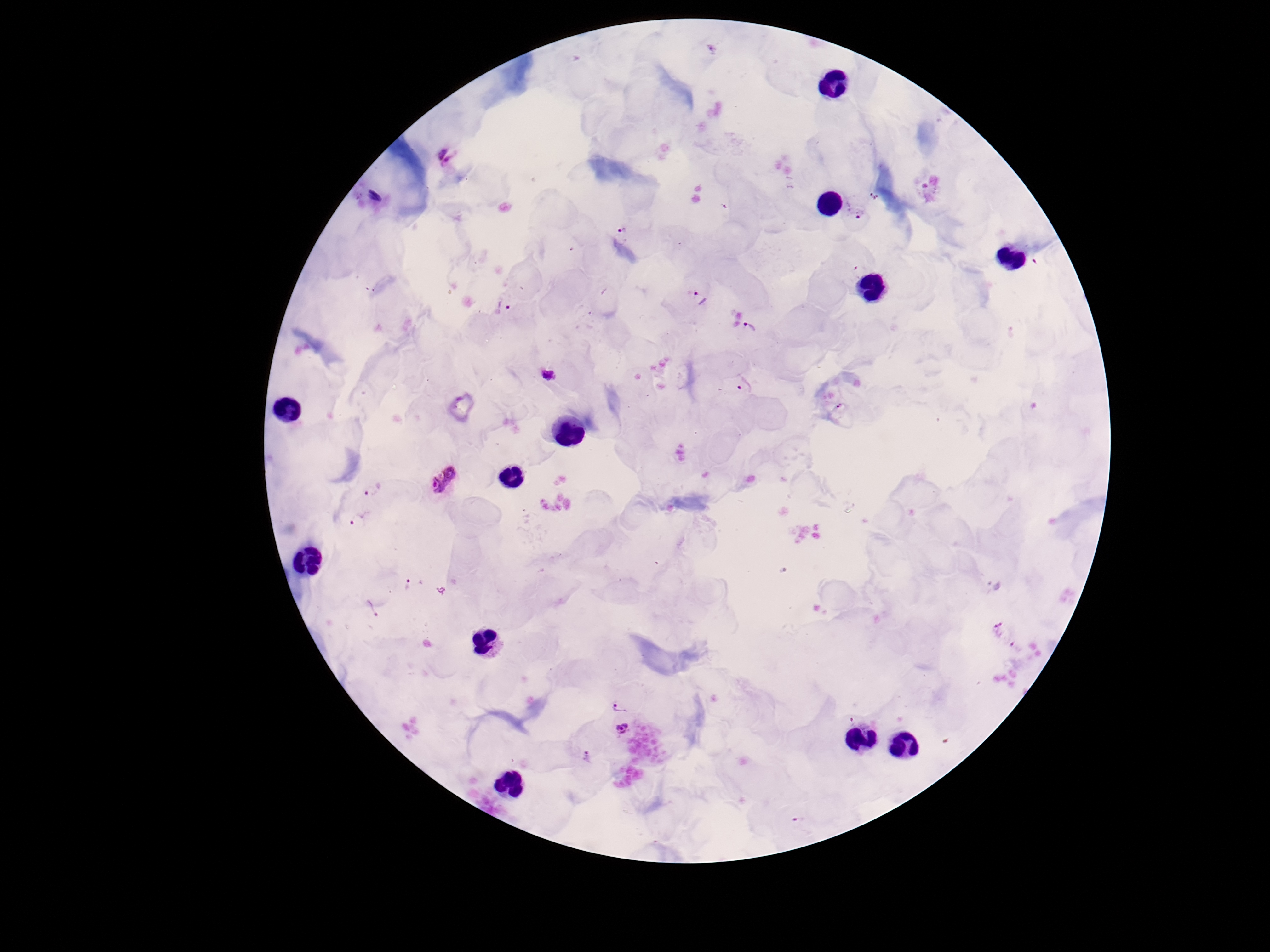
Approximate centers as {x, y} in pixels. Plasmodium parasite locations: {446, 156}, {875, 196}, {860, 212}, {621, 232}, {700, 299}, {505, 307}, {750, 327}, {546, 373}, {745, 385}, {444, 479}, {371, 491}, {358, 521}, {410, 584}, {371, 608}, {998, 630}, {619, 706}, {623, 728}, {587, 756}, {798, 822}. Giemsa stain. Thick peripheral-blood smear. 100x magnification. Image is 1270×952 pixels. Patient malaria status: positive. Single field of view. Photographed through the microscope eyepiece with a smartphone camera.